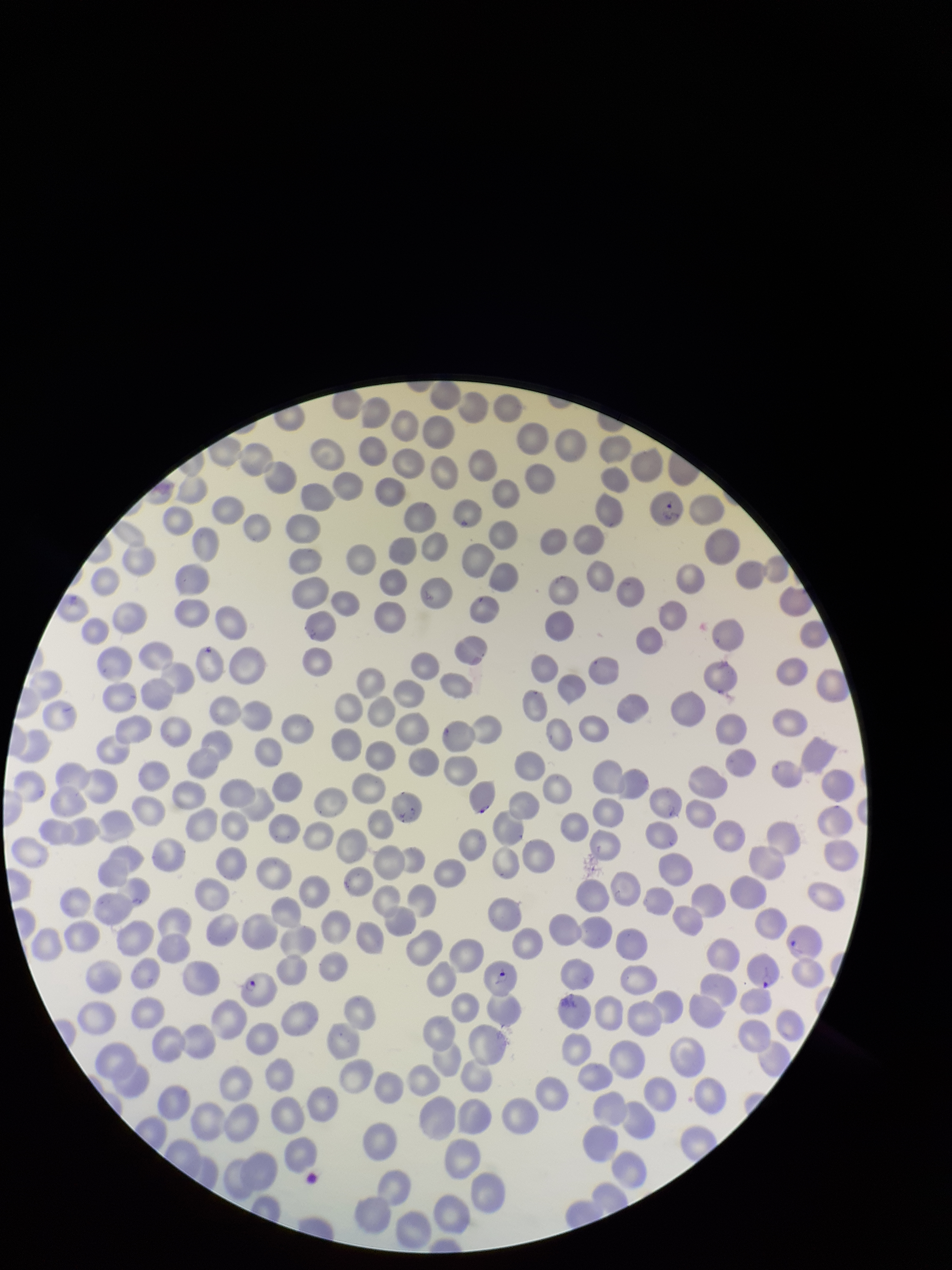
Species reported for this patient: Plasmodium falciparum. Photographed through the microscope eyepiece with a smartphone camera. Red blood cell count: 267. Parasitized red blood cells: identified. Preparation: thin. Image is 952×1270 pixels. Single field of view. Parasitized red blood cell count: 2. Patient malaria status: infected. Stained with Giemsa.